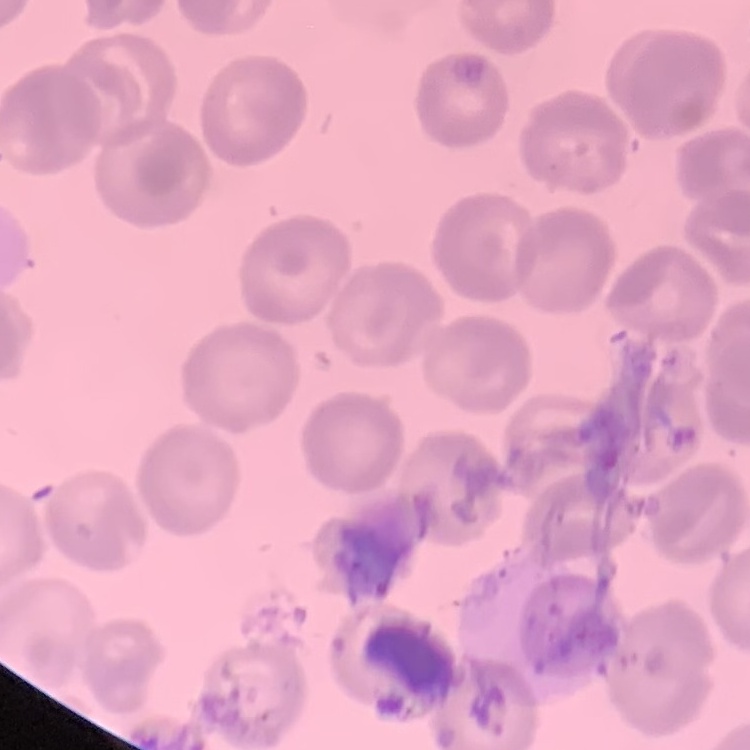 The red blood cells show no rouleaux formation. One tile cut from a larger photomicrograph. Stained with either Field's or Giemsa. Thin blood film.